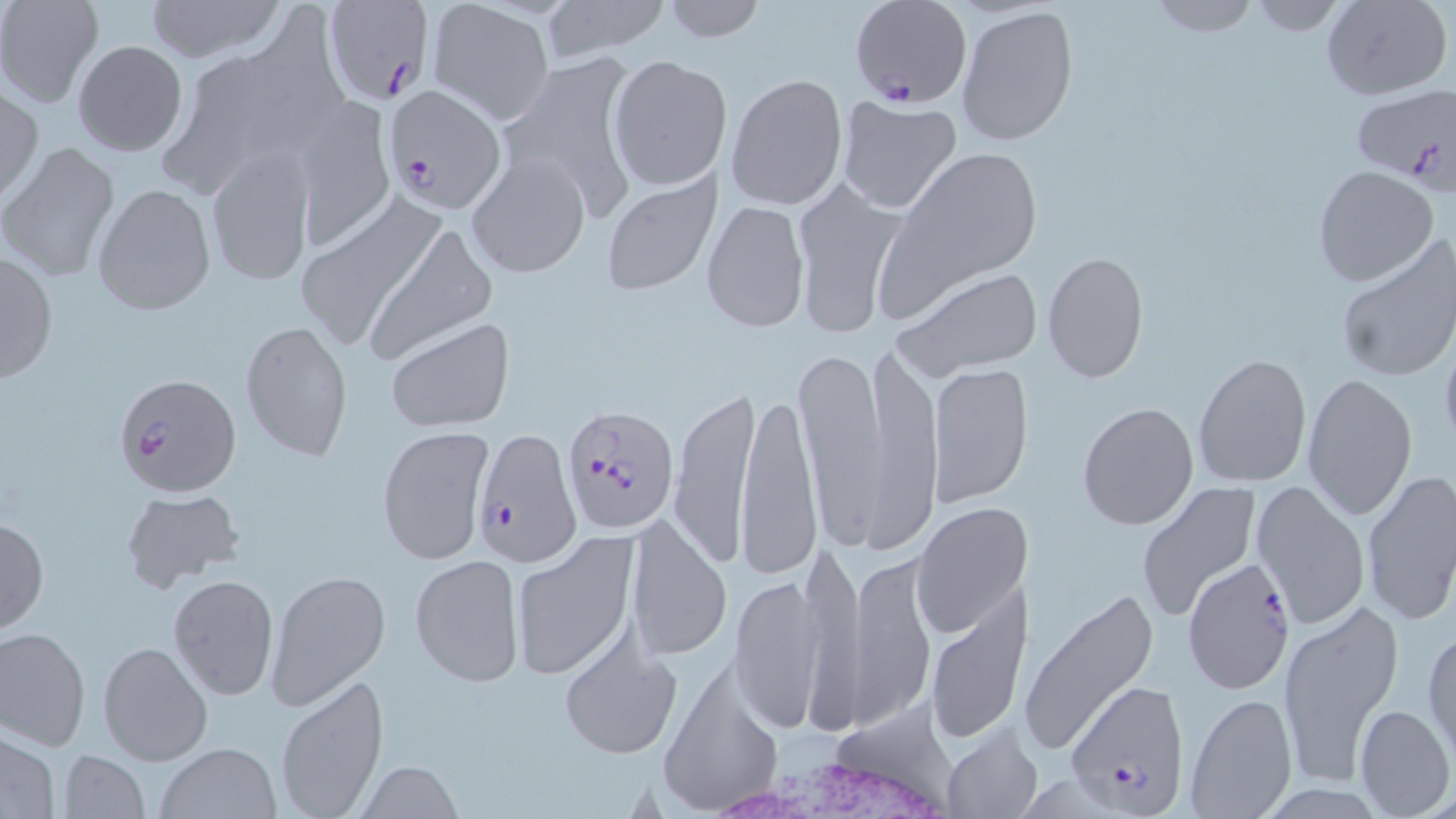

Summary:
  - Coordinate format: approximate bounding boxes as (x1,y1)-(x2,y2) corner pairs in pixels
  - Plasmodium falciparum-infected red blood cell locations: (323,0)-(436,107), (850,0)-(972,110), (386,84)-(507,210), (1354,85)-(1456,188), (112,372)-(242,499), (561,403)-(680,535), (473,430)-(577,567), (1182,556)-(1295,692), (1065,679)-(1190,814)
  - Uninfected red blood cell locations: (0,0)-(103,107), (143,0)-(284,62), (542,0)-(665,61), (658,0)-(767,43), (1146,0)-(1259,37), (1240,0)-(1352,35), (1323,0)-(1453,100), (428,2)-(554,124), (955,4)-(1078,149), (72,39)-(187,157), (498,49)-(645,224), (607,55)-(729,190), (726,73)-(847,209), (0,86)-(43,204), (293,94)-(395,251), (836,95)-(963,213), (1,142)-(122,284), (882,144)-(1044,302), (205,147)-(315,287), (468,152)-(589,278), (1312,164)-(1439,287), (598,168)-(723,297), (789,174)-(908,336), (92,183)-(216,315), (290,193)-(449,352), (703,201)-(809,331), (365,222)-(496,363), (1334,235)-(1455,385), (1,248)-(59,386), (1041,251)-(1150,383), (893,268)-(1043,381), (385,316)-(515,431), (239,318)-(353,463), (1438,329)-(1456,457), (858,340)-(944,543), (796,341)-(899,550), (1192,353)-(1313,487), (927,362)-(1033,507), (1301,372)-(1417,520), (667,383)-(762,569), (737,387)-(823,583), (1077,400)-(1199,530), (376,425)-(494,565), (1359,470)-(1456,628), (1251,479)-(1370,629), (1132,483)-(1261,621), (118,487)-(244,592), (911,503)-(1031,639), (626,514)-(733,664), (0,516)-(49,635), (509,533)-(639,681), (798,534)-(864,715), (850,553)-(935,728), (410,554)-(522,687), (266,569)-(389,708), (168,572)-(280,702), (729,572)-(826,734), (925,591)-(1029,743), (1020,591)-(1158,761), (1277,599)-(1400,792), (1,627)-(91,751), (1424,627)-(1456,764), (557,634)-(682,760), (98,642)-(213,765), (275,673)-(390,817), (1183,691)-(1299,818), (1353,703)-(1454,817), (941,726)-(1043,818), (0,730)-(61,818), (153,741)-(284,819), (56,749)-(150,818), (353,761)-(467,817)
  - White blood cell locations: (704,723)-(978,819)
  - Slide-level diagnosis: Plasmodium falciparum
  - Preparation: thin blood film
  - Magnification: 1000x
  - Stain: May-Grünwald-Giemsa
  - Field of view: single
  - Modality: optical microscopy
  - Image size: 1456×819 pixels